State which parasite is depicted.
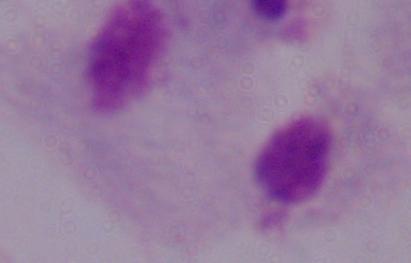
A trichomonad.

magnification = 1000x
modality = micrograph